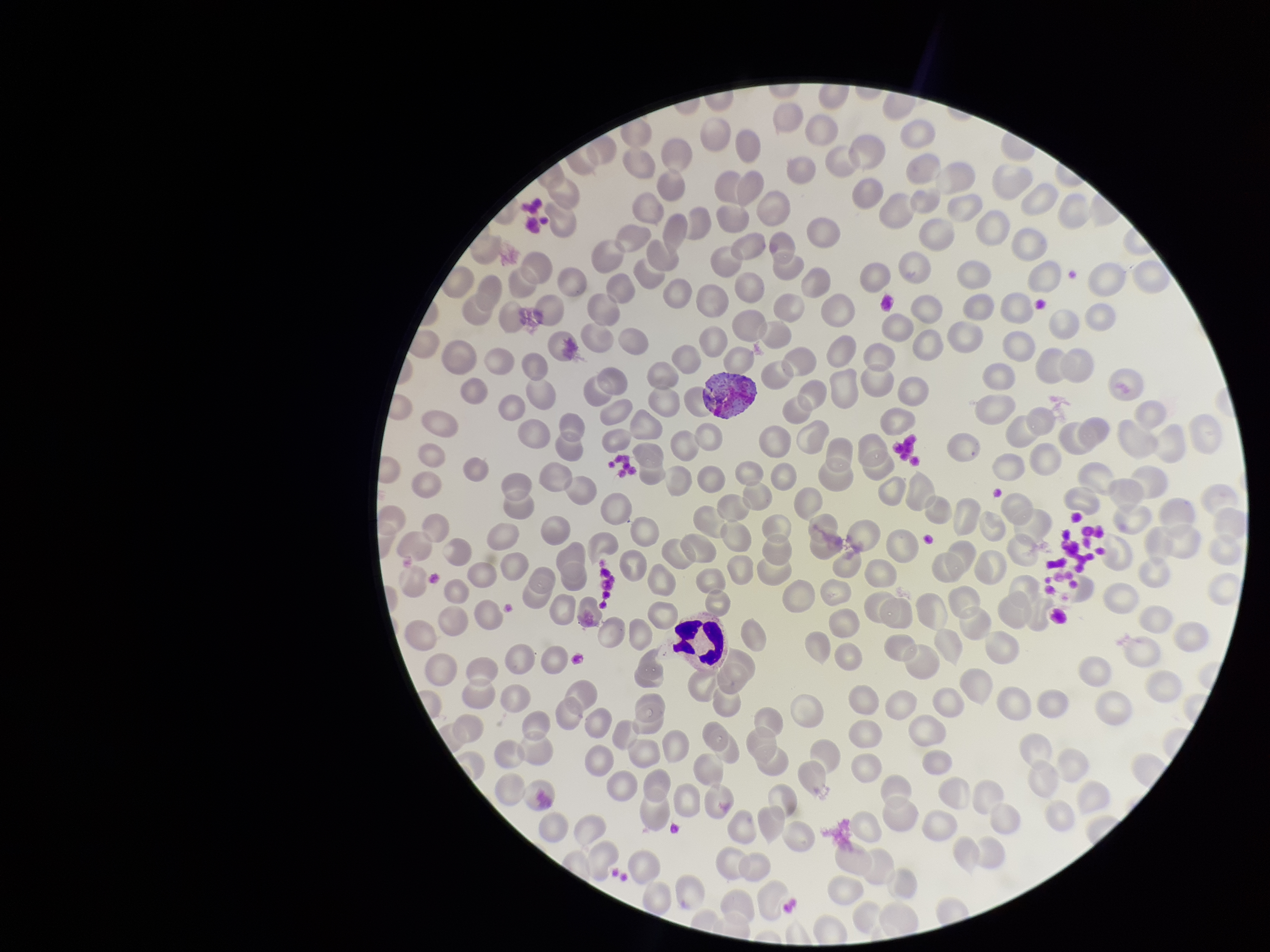

Stained with Giemsa. Parasitized red blood cells: none detected. Image is 1270×952 pixels. Patient malaria status: positive. Species reported for this patient: Plasmodium vivax. Smartphone photograph taken through the eyepiece of a microscope. Single field of view. Red blood cell count: 212. Preparation: thin smear. Parasitized red blood cell count: 0.